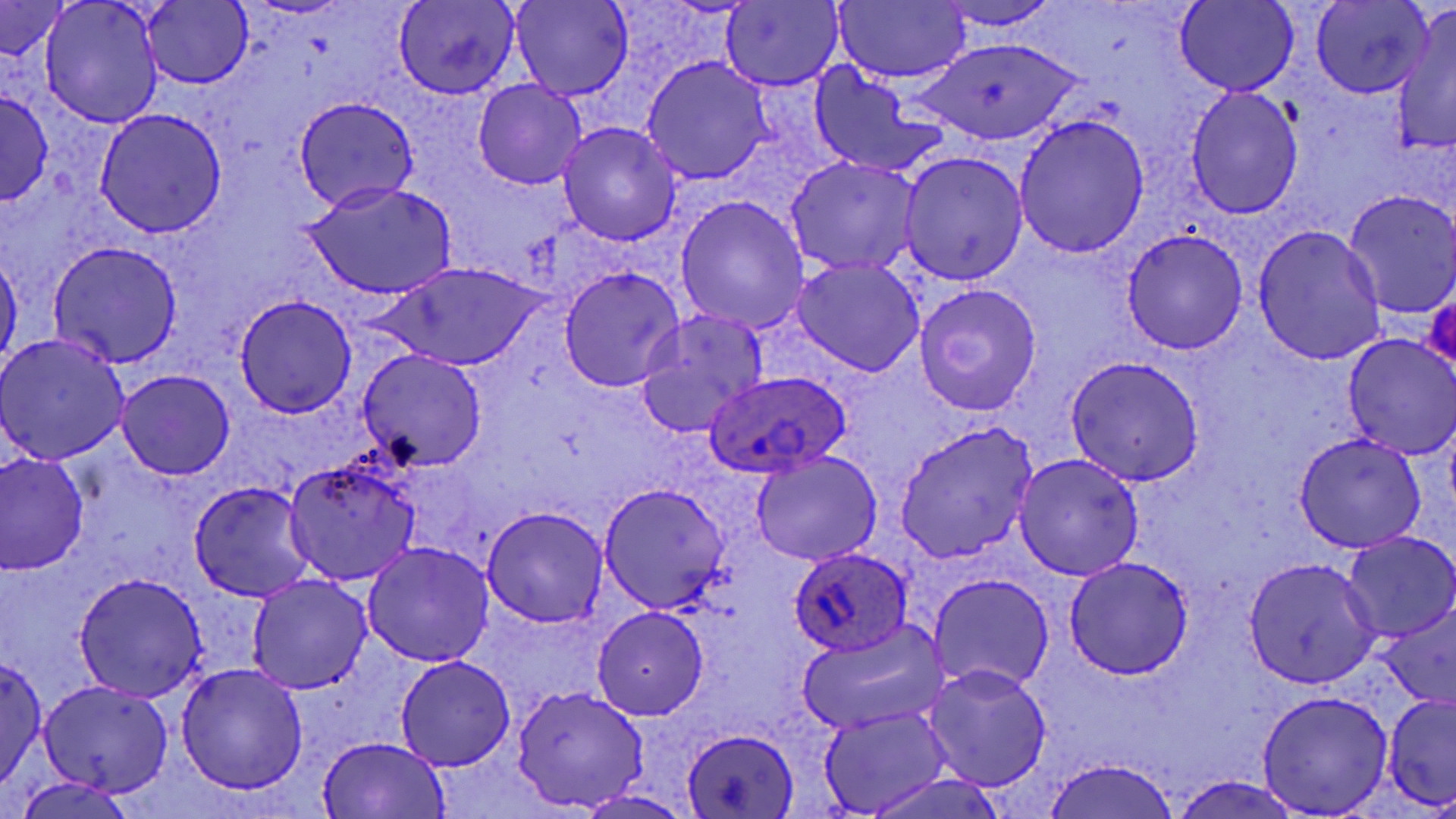
plasmodium_ovale_infected_red_blood_cell_locations: 'approximate bounding boxes as named x1/y1/x2/y2 corners in pixels: (x1=705, y1=370, x2=851, y2=476), (x1=789, y1=547, x2=912, y2=658)'
slide_level_diagnosis: Plasmodium ovale
magnification: 1000x
image_size: 1456×819 pixels
field_of_view: one of a larger specimen
uninfected_red_blood_cell_locations: 'approximate bounding boxes as named x1/y1/x2/y2 corners in pixels: (x1=40, y1=0, x2=163, y2=126), (x1=835, y1=0, x2=970, y2=83), (x1=509, y1=1, x2=634, y2=102), (x1=933, y1=1, x2=1064, y2=31), (x1=1175, y1=1, x2=1298, y2=97), (x1=142, y1=2, x2=252, y2=88), (x1=393, y1=2, x2=520, y2=100), (x1=722, y1=2, x2=844, y2=89), (x1=1311, y1=2, x2=1433, y2=97), (x1=0, y1=3, x2=72, y2=59), (x1=1389, y1=15, x2=1456, y2=159), (x1=913, y1=38, x2=1086, y2=147), (x1=642, y1=57, x2=773, y2=184), (x1=809, y1=65, x2=947, y2=178), (x1=472, y1=78, x2=587, y2=191), (x1=1186, y1=87, x2=1304, y2=219), (x1=1, y1=89, x2=52, y2=204), (x1=293, y1=96, x2=420, y2=212), (x1=94, y1=109, x2=227, y2=237), (x1=1013, y1=114, x2=1150, y2=259), (x1=559, y1=122, x2=682, y2=245), (x1=899, y1=151, x2=1028, y2=284), (x1=784, y1=156, x2=921, y2=275), (x1=305, y1=181, x2=457, y2=299), (x1=1342, y1=190, x2=1456, y2=319), (x1=675, y1=196, x2=809, y2=335), (x1=1252, y1=224, x2=1387, y2=365), (x1=1121, y1=228, x2=1249, y2=354), (x1=49, y1=241, x2=183, y2=368), (x1=0, y1=253, x2=21, y2=371), (x1=794, y1=257, x2=925, y2=377), (x1=381, y1=262, x2=548, y2=370), (x1=560, y1=266, x2=684, y2=392), (x1=912, y1=283, x2=1041, y2=415), (x1=234, y1=295, x2=357, y2=417), (x1=634, y1=310, x2=769, y2=436), (x1=0, y1=333, x2=130, y2=466), (x1=1343, y1=335, x2=1455, y2=458), (x1=358, y1=348, x2=488, y2=472), (x1=1065, y1=355, x2=1205, y2=484), (x1=115, y1=368, x2=236, y2=480), (x1=895, y1=421, x2=1040, y2=562), (x1=1293, y1=433, x2=1426, y2=552), (x1=0, y1=451, x2=89, y2=575), (x1=750, y1=451, x2=883, y2=567), (x1=1013, y1=453, x2=1144, y2=580), (x1=284, y1=458, x2=421, y2=586), (x1=189, y1=481, x2=317, y2=601), (x1=598, y1=484, x2=729, y2=609), (x1=481, y1=507, x2=608, y2=628), (x1=1341, y1=532, x2=1456, y2=640), (x1=363, y1=541, x2=494, y2=666), (x1=1065, y1=556, x2=1195, y2=678), (x1=1245, y1=557, x2=1381, y2=687), (x1=73, y1=574, x2=206, y2=702), (x1=247, y1=575, x2=372, y2=693), (x1=930, y1=576, x2=1053, y2=691), (x1=1376, y1=605, x2=1454, y2=710), (x1=592, y1=607, x2=710, y2=720), (x1=798, y1=619, x2=951, y2=735), (x1=0, y1=655, x2=46, y2=796), (x1=394, y1=656, x2=517, y2=772), (x1=176, y1=662, x2=308, y2=794), (x1=921, y1=664, x2=1053, y2=790), (x1=39, y1=679, x2=174, y2=796), (x1=512, y1=686, x2=646, y2=812), (x1=1257, y1=690, x2=1393, y2=816), (x1=1383, y1=693, x2=1456, y2=809), (x1=818, y1=707, x2=952, y2=816), (x1=682, y1=728, x2=800, y2=817), (x1=318, y1=736, x2=450, y2=817), (x1=1042, y1=757, x2=1182, y2=819), (x1=862, y1=769, x2=1007, y2=819), (x1=1170, y1=775, x2=1305, y2=818), (x1=14, y1=776, x2=135, y2=819), (x1=576, y1=790, x2=694, y2=819)'
stain: May-Grünwald-Giemsa
preparation: thin blood film
modality: optical microscopy